State which parasite is depicted.
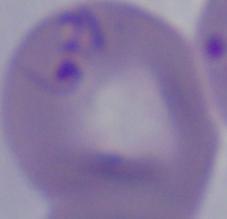
This is Babesia.

Summary:
  - Magnification: 1000x
  - Modality: micrograph